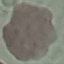 Result: no malaria parasites detected. Acquired by smartphone through the microscope eyepiece. Thin blood film. Cell patch, automatically extracted from a larger field of view and resized to 64 × 64 pixels. Giemsa stain.